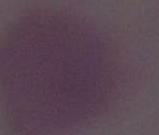
Captured at 1000x magnification. Micrograph. An erythrocyte is seen.